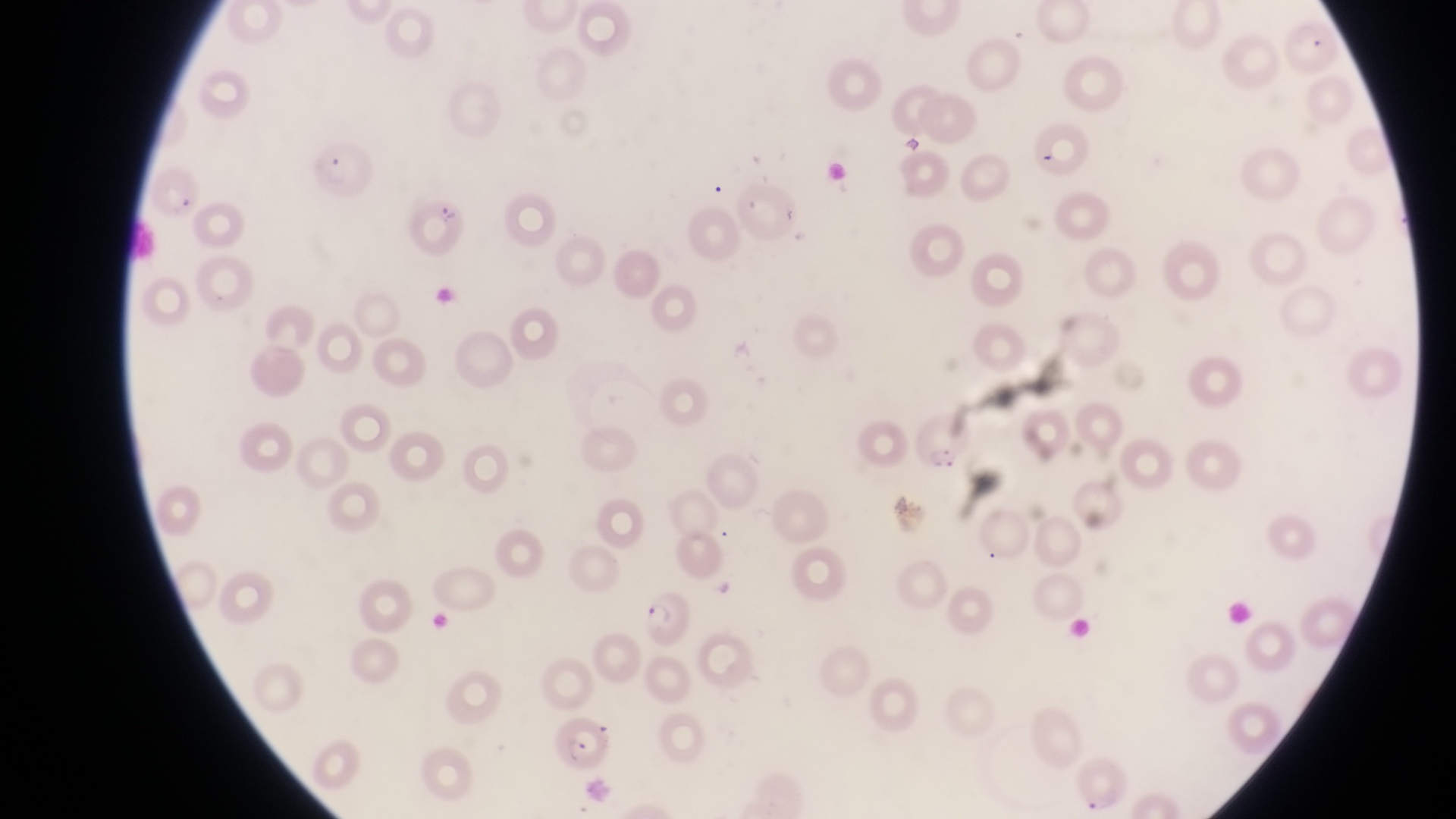

Approximate bounding boxes as [left, top, right, bottom] in pixels.
Summary:
  - Parasitised red blood cell locations: [315, 146, 374, 201], [146, 168, 202, 220], [402, 195, 469, 253], [915, 409, 974, 470], [635, 594, 695, 649], [548, 719, 612, 774]
  - Magnification: 1000x
  - Field of view: single
  - Preparation: thin blood film
  - Image size: 1456×819 pixels
  - Country: Uganda
  - Capture: smartphone photograph through the eyepiece of an Olympus CX-23 microscope